Point out Plasmodium parasites and leukocytes.
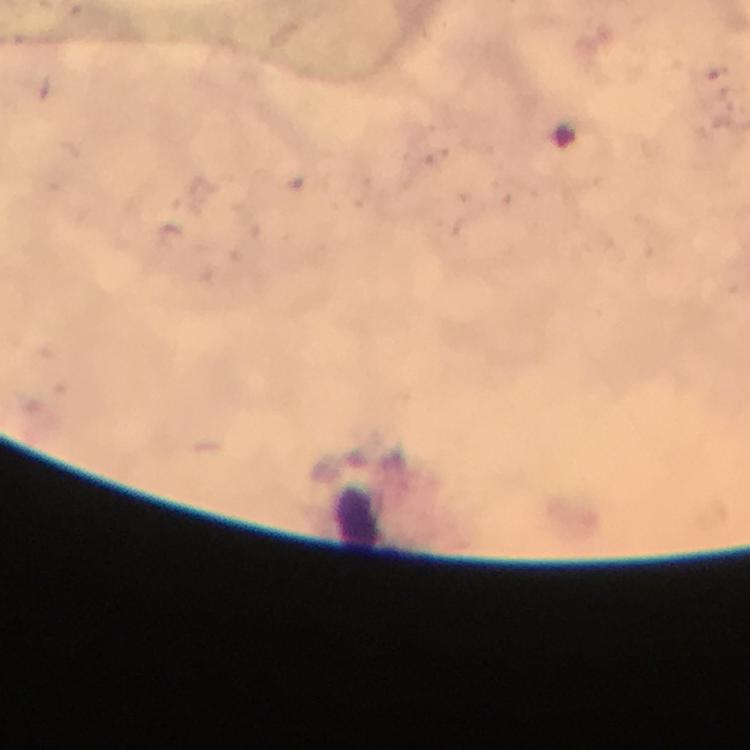

No Plasmodium parasites seen.
Approximate centers as {x, y} in pixels.
Leukocytes: {358, 520}.

Summary:
  - Cropped from: one field of view
  - Preparation: thick blood film
  - Stain: Giemsa
  - Magnification: 100x
  - Immersion oil: applied
  - Image size: 750×750 pixels
  - Context: from a malaria diagnostic workup
  - Capture: smartphone camera through the microscope